Classify this cell by malaria status.
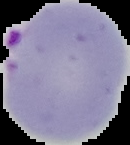

It is parasitized.

image_type: segmented cell region on a black background
image_size: 130×145 pixels
preparation: thin blood film